Identify the parasite.
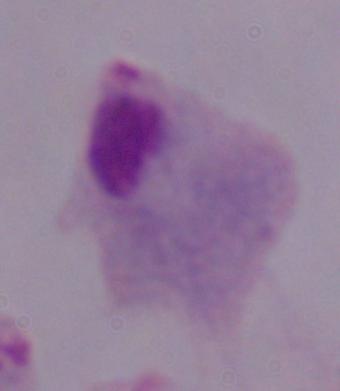
This is a trichomonad.

magnification = 1000x
modality = micrograph